State which cell type is depicted.
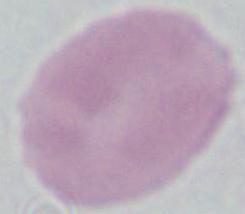

An erythrocyte.

magnification = 1000x
modality = micrograph